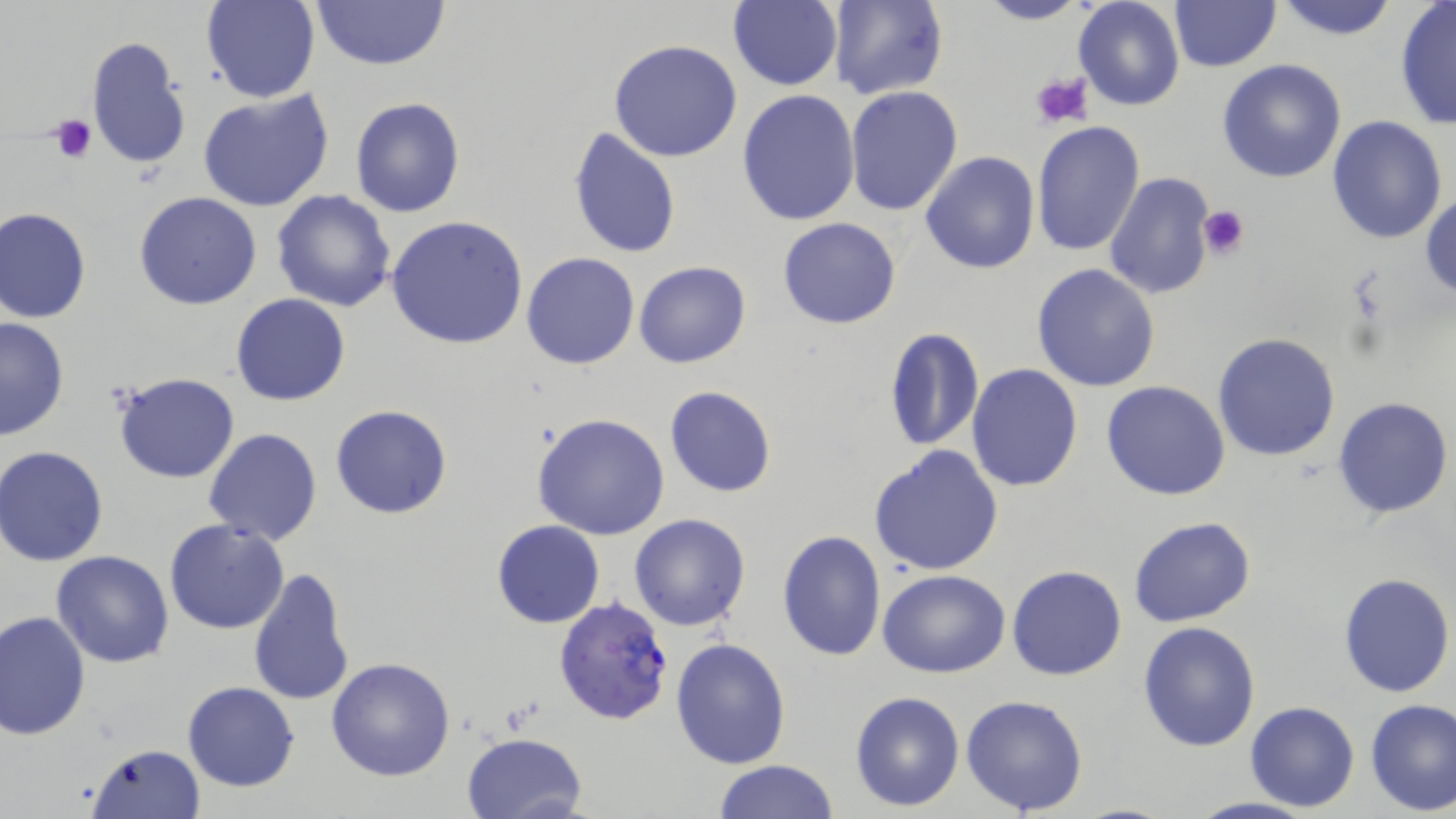

plasmodium_falciparum_infected_red_blood_cell_locations: 'approximate bounding boxes as (x1, y1, x2, y2) in pixels: (553, 594, 675, 727)'
slide_level_diagnosis: Plasmodium falciparum
stain: May-Grünwald-Giemsa
field_of_view: single
preparation: thin blood film
modality: optical microscopy
uninfected_red_blood_cell_locations: 'approximate bounding boxes as (x1, y1, x2, y2) in pixels: (202, 0, 320, 104), (308, 0, 452, 73), (828, 0, 947, 101), (971, 0, 1093, 25), (1272, 0, 1403, 40), (726, 1, 843, 89), (1074, 1, 1186, 111), (1171, 2, 1280, 71), (1394, 2, 1456, 132), (85, 36, 191, 171), (609, 39, 743, 163), (1217, 59, 1348, 184), (845, 85, 963, 216), (196, 88, 336, 212), (735, 89, 861, 228), (350, 97, 465, 218), (1327, 115, 1448, 245), (1030, 120, 1144, 256), (568, 125, 682, 260), (919, 152, 1040, 275), (1103, 171, 1217, 302), (1420, 190, 1455, 303), (271, 191, 396, 312), (134, 192, 261, 310), (1, 207, 92, 323), (386, 215, 529, 350), (777, 217, 903, 329), (521, 252, 639, 369), (633, 261, 752, 368), (1032, 263, 1162, 392), (230, 294, 351, 406), (0, 317, 70, 442), (881, 326, 983, 454), (1213, 333, 1342, 462), (967, 364, 1083, 491), (112, 372, 241, 483), (1101, 381, 1231, 501), (664, 386, 776, 498), (1332, 394, 1454, 520), (331, 404, 454, 520), (532, 413, 672, 539), (203, 428, 323, 547), (867, 444, 1006, 575), (1, 446, 113, 565), (628, 513, 751, 632), (1129, 517, 1256, 627), (491, 519, 605, 629), (164, 520, 290, 635), (776, 530, 887, 662), (51, 550, 174, 668), (1007, 565, 1127, 681), (248, 567, 355, 707), (877, 569, 1010, 678), (1338, 571, 1454, 697), (0, 609, 91, 740), (1137, 620, 1261, 753), (670, 637, 791, 769), (326, 657, 456, 780), (181, 681, 300, 793), (849, 690, 964, 812), (960, 693, 1089, 816), (1365, 699, 1456, 815), (1245, 701, 1360, 812), (460, 731, 587, 819), (84, 742, 204, 819), (713, 759, 839, 818), (1185, 796, 1319, 819)'
platelet_locations: 'approximate bounding boxes as (x1, y1, x2, y2) in pixels: (1030, 71, 1094, 130), (47, 114, 96, 164), (1199, 206, 1251, 259)'
image_size: 1456×819 pixels
magnification: 1000x